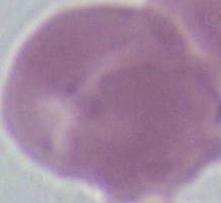
identification: erythrocyte
modality: micrograph
magnification: 1000x